Report the malaria status of this cell.
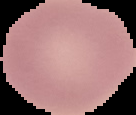
It is uninfected.

Summary:
  - Image type: segmented cell region on a black background
  - Image size: 136×115 pixels
  - Preparation: thin blood film